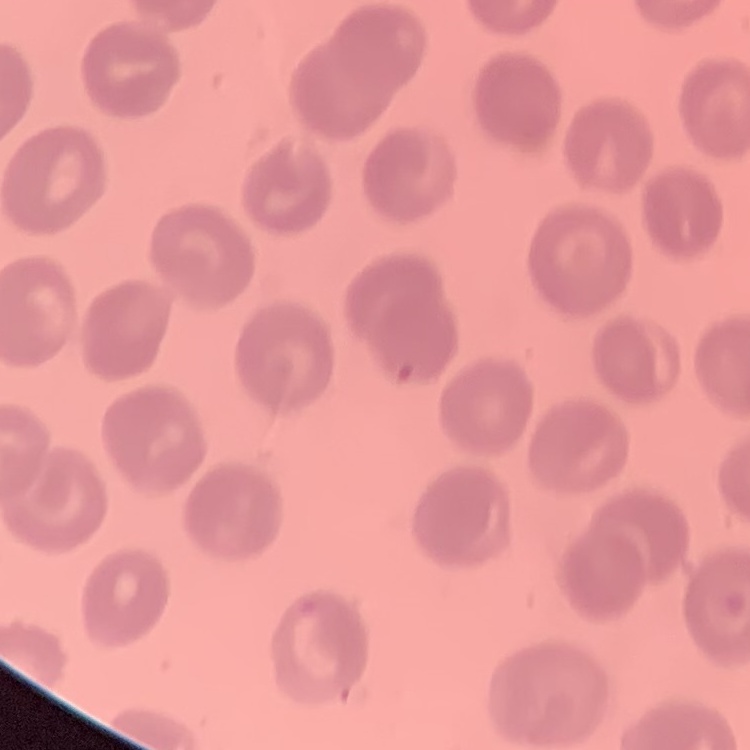

Summary:
  - Red blood cell morphology: no rouleaux formation
  - Stain: Field's or Giemsa
  - Image type: one tile cut from a larger photomicrograph
  - Preparation: thin peripheral smear